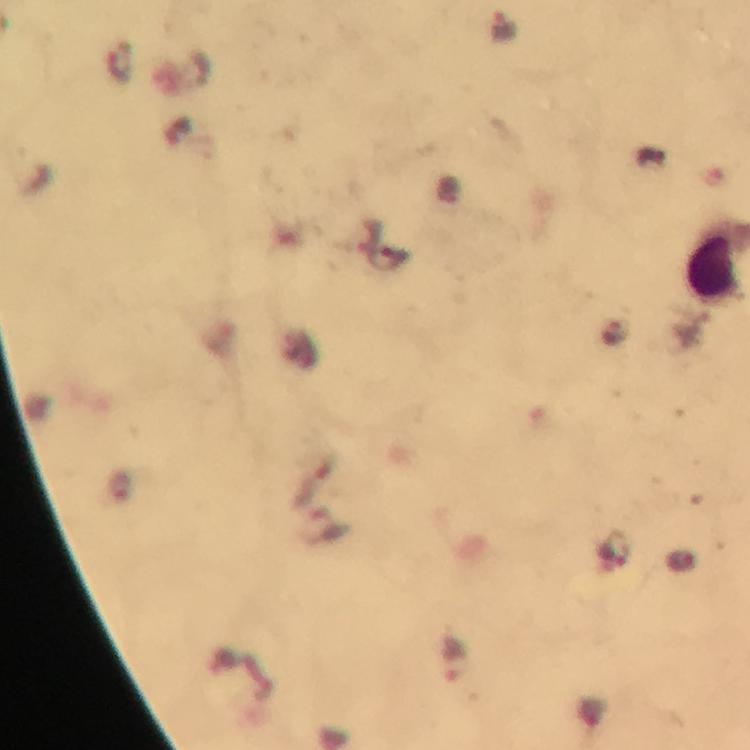
Approximate centers as {x, y} in pixels. Leukocyte locations: {714, 263}. Malaria parasite locations: {503, 24}, {616, 549}, {455, 660}. Immersion oil applied. Thick blood film. Image is 750×750 pixels. 100x magnification. A crop from one field of view. Giemsa-stained preparation. From a malaria diagnostic workup. Photographed through the microscope with a smartphone camera.